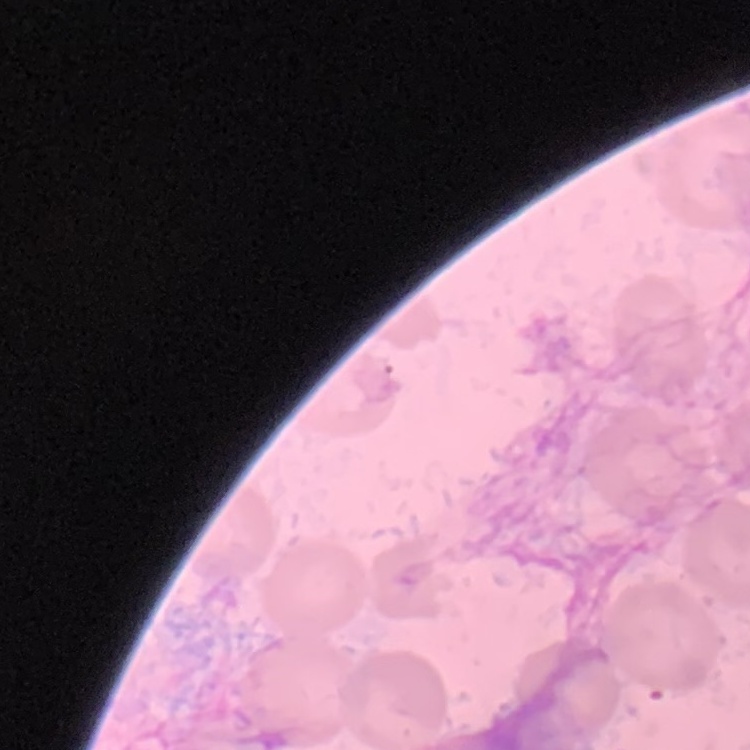
erythrocyte morphology = no rouleaux formation
preparation = thin blood smear
stain = Field's or Giemsa
image type = one tile cut from a larger photomicrograph